Locate every Plasmodium parasite.
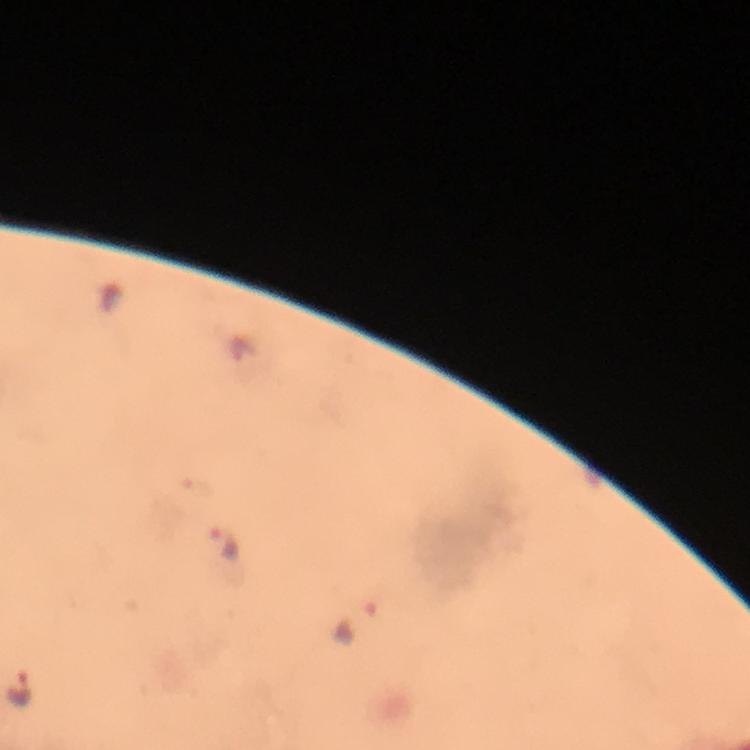
Approximate centers as (x, y) in pixels.
Plasmodium parasites: (223, 542), (358, 624), (18, 690).

Giemsa stain. Cropped region of a single field of view. Smartphone photograph taken through a microscope. Thick blood film. 100x magnification. Image is 750×750 pixels. Immersion oil was used. From a malaria diagnostic workup.